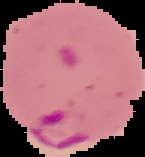

Summary:
  - Result: malaria parasites identified
  - Image size: 145×157 pixels
  - Preparation: thin blood smear
  - Image type: segmented cell region on a black background